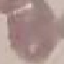

Summary:
  - Malaria status: uninfected
  - Stain: Giemsa
  - Image type: automatically extracted cell patch, resized to 64 × 64 pixels
  - Preparation: thin smear
  - Capture: smartphone through the microscope eyepiece